Classify this cell by malaria status.
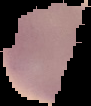

It is uninfected.

Summary:
  - Image type: segmented cell region with the area outside set to black
  - Image size: 91×106 pixels
  - Preparation: thin blood smear